Outline each blood parasite and name the species.
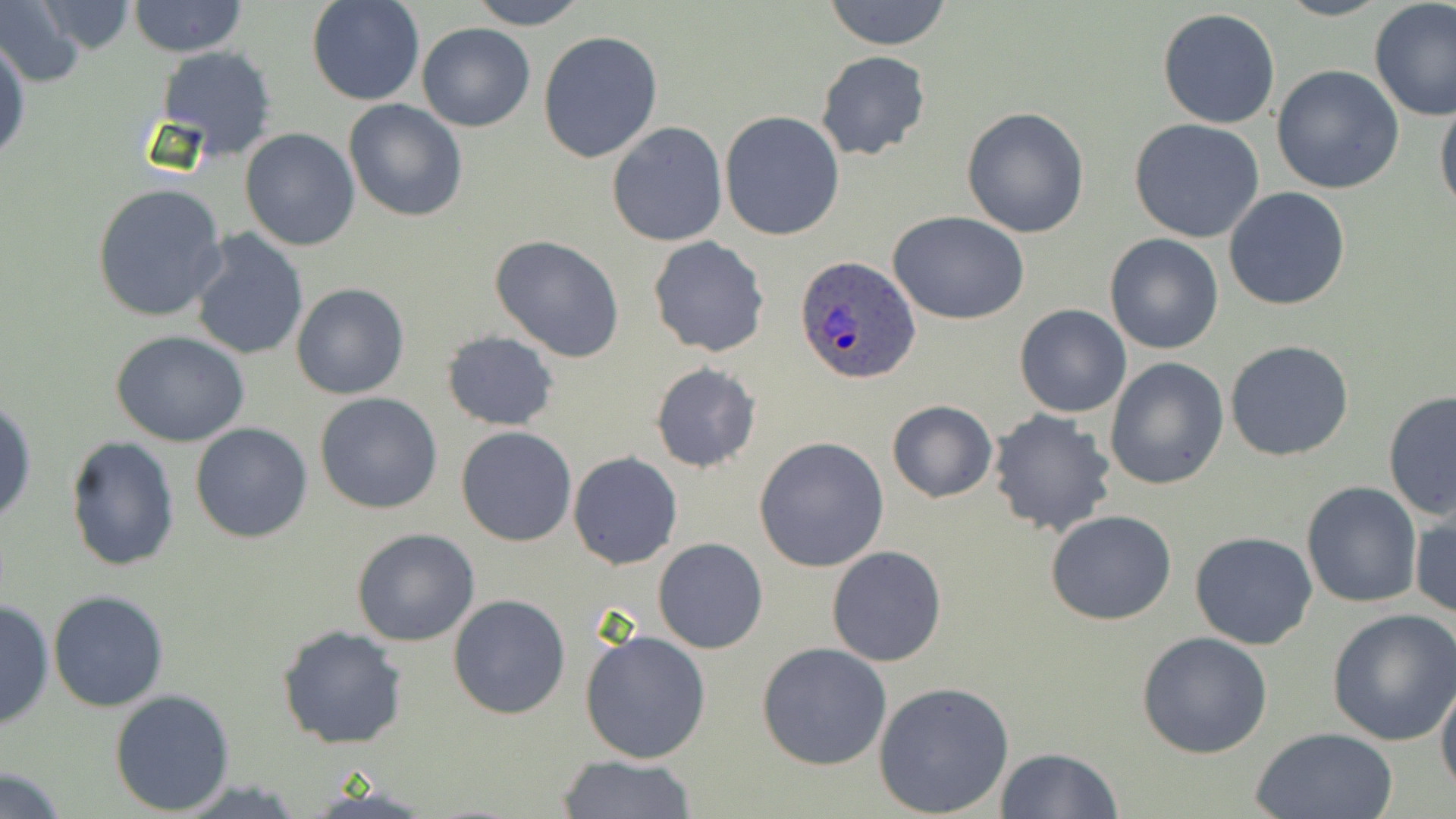
Approximate bounding boxes as [x1, y1, x2, y2] in pixels.
Plasmodium ovale-infected red blood cells: [794, 255, 922, 386].
No Plasmodium falciparum, Plasmodium malariae, Plasmodium vivax, Babesia divergens, or Trypanosoma brucei observed.

Summary:
  - Uninfected red blood cell locations: [0, 0, 88, 89], [306, 0, 425, 106], [467, 0, 588, 29], [822, 0, 953, 51], [1368, 0, 1456, 120], [28, 1, 144, 57], [128, 1, 247, 58], [1157, 8, 1282, 129], [417, 23, 535, 132], [538, 30, 665, 163], [1, 32, 29, 164], [154, 46, 279, 161], [816, 50, 930, 161], [1270, 65, 1404, 194], [1434, 96, 1456, 219], [343, 99, 470, 222], [961, 107, 1090, 238], [720, 110, 845, 241], [1129, 118, 1267, 244], [607, 123, 728, 247], [240, 127, 361, 250], [92, 182, 228, 324], [1223, 187, 1351, 311], [889, 212, 1029, 325], [187, 230, 309, 360], [1102, 233, 1225, 355], [491, 234, 625, 361], [647, 237, 770, 357], [292, 283, 409, 400], [1014, 304, 1132, 418], [440, 329, 561, 431], [110, 330, 252, 446], [1225, 340, 1354, 462], [1104, 357, 1229, 489], [649, 361, 763, 474], [1382, 390, 1456, 523], [315, 392, 442, 513], [1, 398, 36, 527], [886, 398, 998, 504], [987, 409, 1118, 539], [189, 422, 313, 544], [456, 427, 578, 547], [63, 435, 181, 574], [755, 436, 890, 573], [568, 451, 683, 570], [1301, 480, 1422, 609], [1411, 508, 1455, 622], [1046, 510, 1176, 626], [351, 528, 480, 647], [1190, 531, 1317, 649], [653, 538, 768, 654], [827, 546, 947, 666], [48, 589, 170, 712], [447, 593, 571, 720], [0, 597, 53, 731], [1327, 608, 1456, 745], [278, 625, 407, 750], [579, 627, 711, 764], [1136, 631, 1274, 758], [757, 642, 891, 771], [1435, 673, 1456, 797], [874, 679, 1014, 817], [109, 688, 235, 813], [1250, 727, 1399, 818], [993, 747, 1123, 818], [557, 755, 698, 817], [0, 766, 71, 819]
  - Slide-level diagnosis: Plasmodium ovale
  - Magnification: 1000x
  - Field of view: single
  - Modality: light microscopy
  - Stain: May-Grünwald-Giemsa
  - Preparation: thin blood smear
  - Image size: 1456×819 pixels